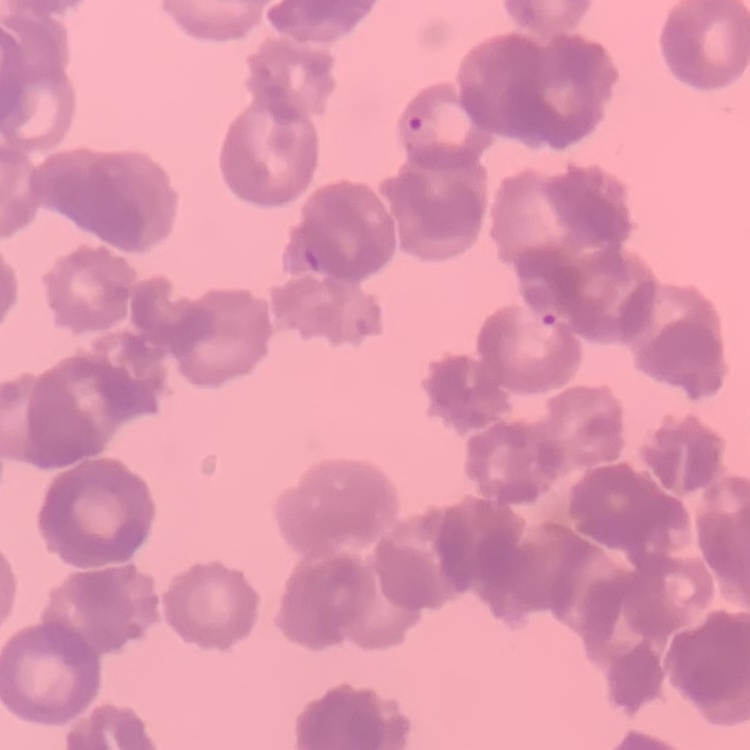 The erythrocytes show rouleaux formation. Square crop of a larger photomicrograph. Thin peripheral smear. Field's or Giemsa stain.